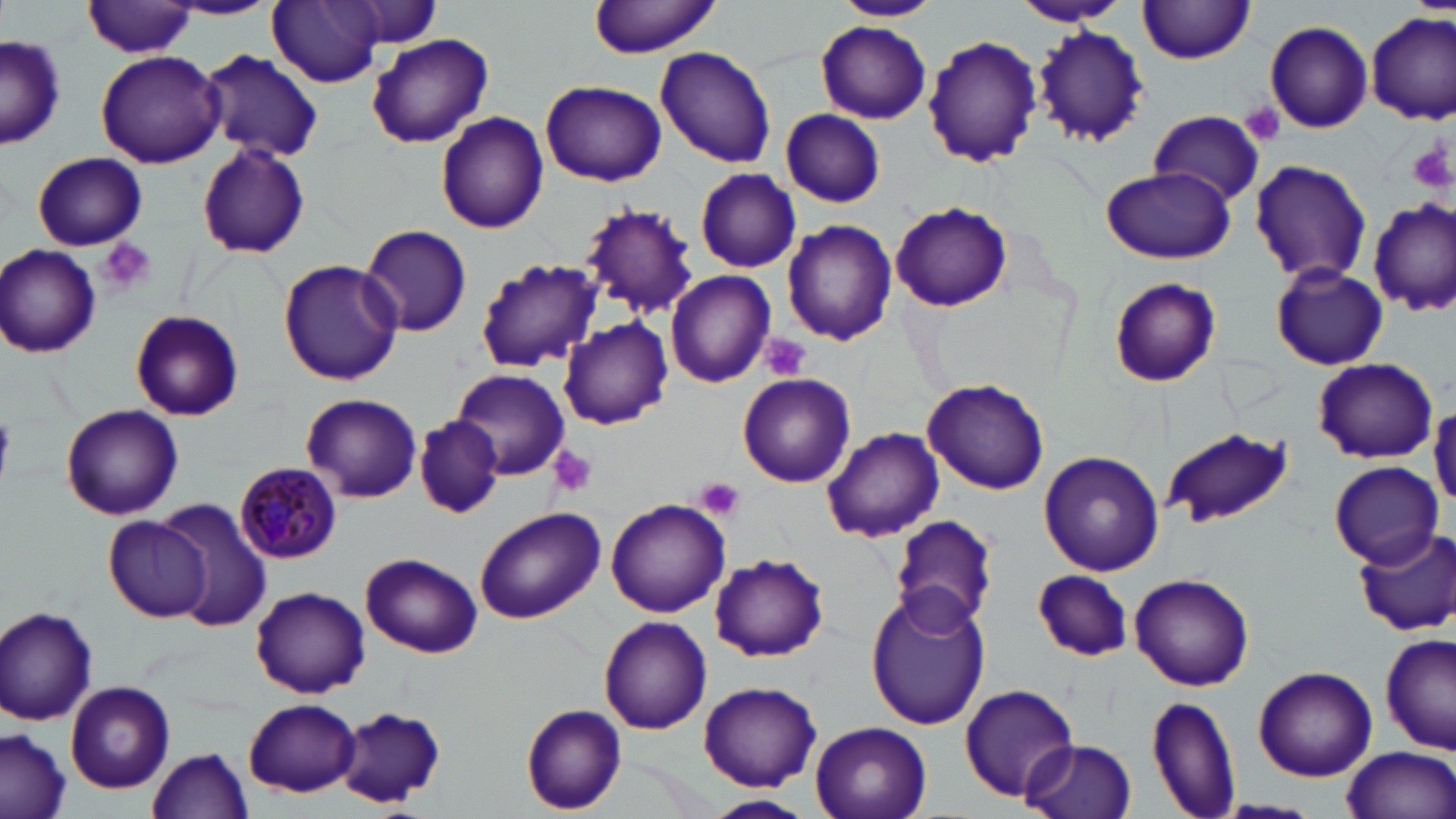
Summary:
  - Coordinate format: approximate bounding boxes as (x1,y1)-(x2,y2) corner pairs in pixels
  - Uninfected red blood cell locations: (588,0)-(725,58), (831,0)-(941,23), (1011,0)-(1128,27), (166,1)-(282,20), (267,1)-(385,87), (330,1)-(444,53), (1138,1)-(1256,64), (83,2)-(200,58), (1366,10)-(1455,124), (1263,20)-(1375,133), (816,21)-(933,123), (1032,23)-(1149,147), (366,33)-(493,148), (923,34)-(1045,168), (1,35)-(64,151), (654,45)-(776,168), (199,49)-(323,162), (94,50)-(226,169), (541,78)-(667,186), (780,109)-(885,207), (1148,109)-(1266,203), (436,111)-(549,233), (197,141)-(311,260), (31,152)-(147,251), (1249,160)-(1374,285), (1101,164)-(1235,266), (695,169)-(801,273), (1370,200)-(1455,316), (891,202)-(1011,311), (580,205)-(698,320), (782,219)-(900,345), (360,223)-(472,337), (1,245)-(101,359), (475,258)-(602,374), (277,259)-(404,387), (1270,263)-(1388,371), (664,269)-(775,388), (1107,277)-(1221,387), (129,309)-(244,422), (558,317)-(672,429), (1311,357)-(1438,464), (451,366)-(572,480), (737,374)-(856,486), (922,377)-(1050,495), (301,393)-(423,502), (1430,402)-(1456,511), (59,404)-(183,520), (414,416)-(505,519), (822,427)-(944,544), (1162,427)-(1294,527), (1037,449)-(1165,576), (1327,460)-(1443,567), (606,498)-(730,617), (158,500)-(271,628), (474,506)-(606,624), (890,514)-(999,631), (104,516)-(213,620), (1351,527)-(1454,637), (361,552)-(483,657), (708,552)-(829,662), (1033,569)-(1135,660), (1130,571)-(1255,690), (250,585)-(370,698), (863,588)-(992,733), (0,606)-(98,725), (598,614)-(713,734), (1381,633)-(1455,754), (1253,666)-(1377,781), (64,681)-(175,793), (698,681)-(822,790), (957,683)-(1081,804), (1145,693)-(1242,819), (242,699)-(362,796), (520,704)-(627,814), (334,707)-(446,810), (810,721)-(932,819), (0,730)-(71,819), (1023,738)-(1137,819), (1341,745)-(1454,819), (147,748)-(253,819), (702,793)-(817,818), (1211,799)-(1323,818)
  - Platelet locations: (1238,102)-(1285,145), (1409,138)-(1454,193), (97,238)-(156,295), (759,334)-(813,382), (0,410)-(13,481), (546,444)-(599,498), (696,477)-(746,520)
  - Plasmodium malariae-infected red blood cell locations: (234,462)-(343,564)
  - Slide-level diagnosis: Plasmodium malariae
  - Modality: optical microscopy
  - Preparation: thin blood smear
  - Magnification: 1000x
  - Field of view: single
  - Stain: May-Grünwald-Giemsa
  - Image size: 1456×819 pixels